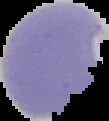
The area outside the segmented cell region is set to black. From a thin blood smear. Image is 109×121 pixels. Malaria status: parasitized.